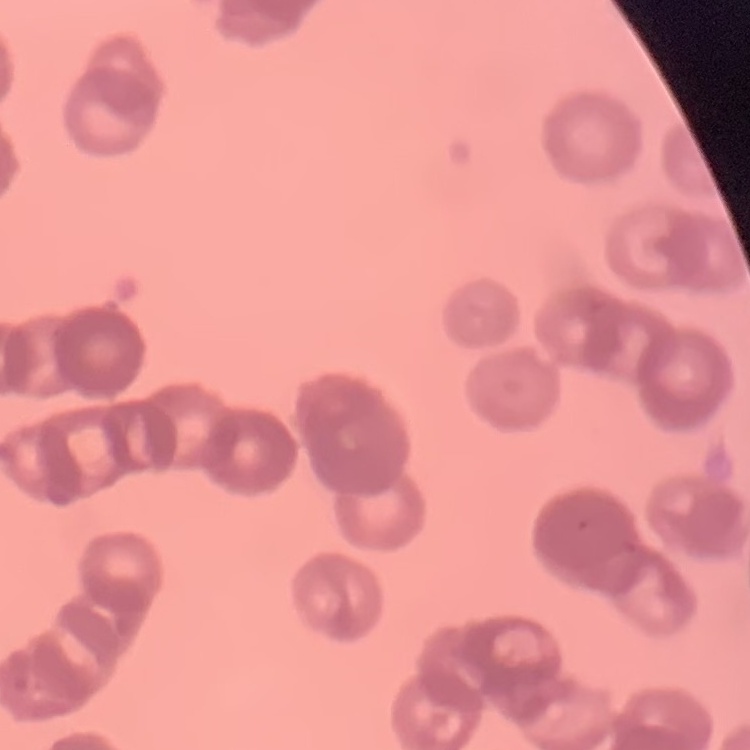 The erythrocytes show rouleaux formation. Thin blood film. Square crop of a larger photomicrograph. Field's or Giemsa stain.